State the blood parasite species.
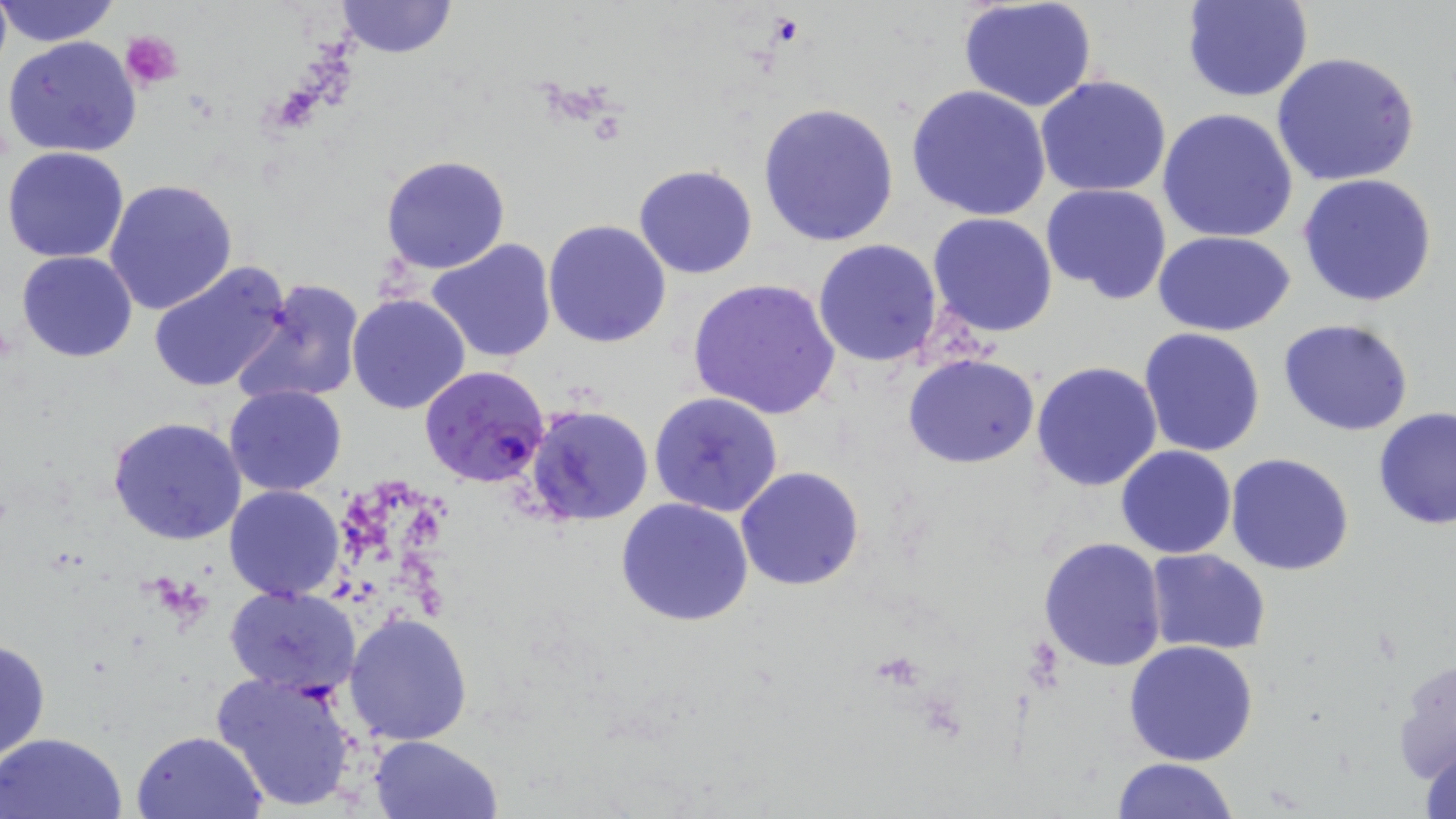
Plasmodium falciparum.

Approximate bounding boxes as named x1/y1/x2/y2 corners in pixels. Plasmodium falciparum-infected red blood cell locations: (x1=419, y1=365, x2=551, y2=487). Platelet locations: (x1=769, y1=15, x2=805, y2=45), (x1=123, y1=29, x2=185, y2=89). Uninfected red blood cell locations: (x1=0, y1=0, x2=122, y2=48), (x1=1182, y1=0, x2=1313, y2=103), (x1=333, y1=1, x2=457, y2=58), (x1=957, y1=2, x2=1099, y2=113), (x1=4, y1=35, x2=142, y2=159), (x1=1273, y1=52, x2=1421, y2=186), (x1=1035, y1=76, x2=1173, y2=199), (x1=905, y1=83, x2=1052, y2=222), (x1=757, y1=103, x2=900, y2=249), (x1=1156, y1=109, x2=1299, y2=246), (x1=3, y1=145, x2=131, y2=263), (x1=380, y1=154, x2=512, y2=274), (x1=633, y1=165, x2=759, y2=279), (x1=1298, y1=174, x2=1439, y2=307), (x1=105, y1=179, x2=238, y2=317), (x1=1041, y1=183, x2=1172, y2=304), (x1=927, y1=212, x2=1059, y2=339), (x1=544, y1=220, x2=672, y2=348), (x1=1153, y1=232, x2=1296, y2=338), (x1=426, y1=238, x2=557, y2=363), (x1=812, y1=239, x2=943, y2=368), (x1=15, y1=251, x2=139, y2=363), (x1=148, y1=261, x2=294, y2=394), (x1=232, y1=278, x2=365, y2=408), (x1=687, y1=278, x2=842, y2=420), (x1=347, y1=293, x2=472, y2=413), (x1=1278, y1=319, x2=1417, y2=437), (x1=1137, y1=328, x2=1267, y2=457), (x1=903, y1=354, x2=1041, y2=470), (x1=1031, y1=361, x2=1162, y2=491), (x1=224, y1=385, x2=346, y2=497), (x1=649, y1=392, x2=783, y2=518), (x1=526, y1=405, x2=654, y2=527), (x1=1373, y1=408, x2=1456, y2=531), (x1=106, y1=415, x2=248, y2=546), (x1=1116, y1=446, x2=1237, y2=560), (x1=1225, y1=452, x2=1356, y2=575), (x1=735, y1=466, x2=865, y2=591), (x1=225, y1=485, x2=345, y2=601), (x1=615, y1=497, x2=754, y2=627), (x1=1038, y1=536, x2=1167, y2=671), (x1=1145, y1=549, x2=1273, y2=656), (x1=224, y1=585, x2=362, y2=694), (x1=344, y1=611, x2=474, y2=744), (x1=0, y1=637, x2=50, y2=764), (x1=1123, y1=640, x2=1259, y2=766), (x1=1390, y1=655, x2=1455, y2=790), (x1=210, y1=670, x2=363, y2=813), (x1=133, y1=729, x2=267, y2=817), (x1=1, y1=731, x2=128, y2=819), (x1=370, y1=734, x2=502, y2=819), (x1=1414, y1=738, x2=1456, y2=819), (x1=1112, y1=757, x2=1238, y2=818). Single field of view. 1000x magnification. Light microscopy. Thin blood smear. May-Grünwald-Giemsa stain. Image is 1456×819 pixels.